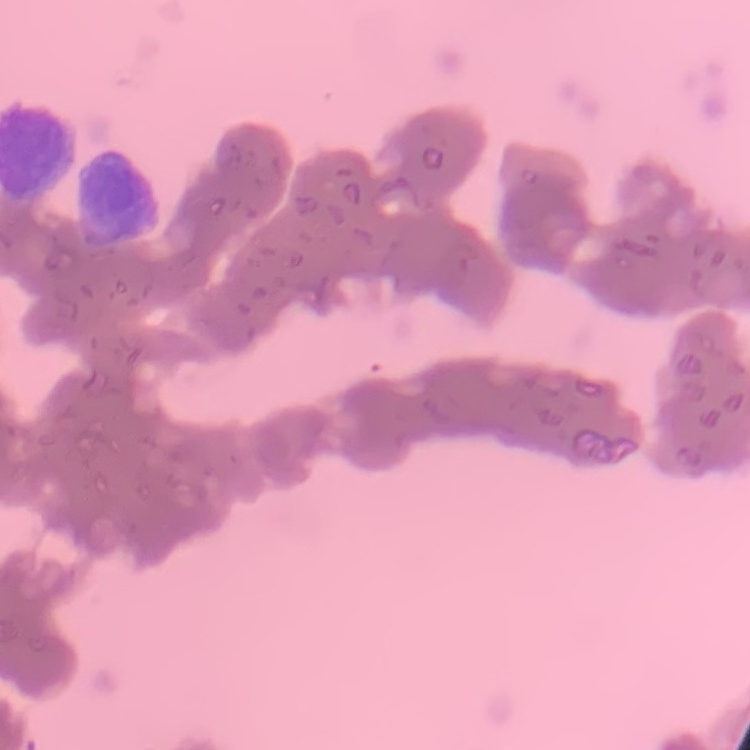
The erythrocytes exhibit rouleaux formation. Square crop of a larger photomicrograph. Thin peripheral smear. Stained with either Field's or Giemsa.